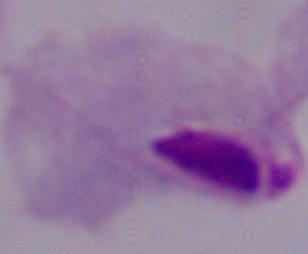

Summary:
  - Modality: micrograph
  - Magnification: 1000x
  - Identification: trichomonad